Give the position of every malaria parasite.
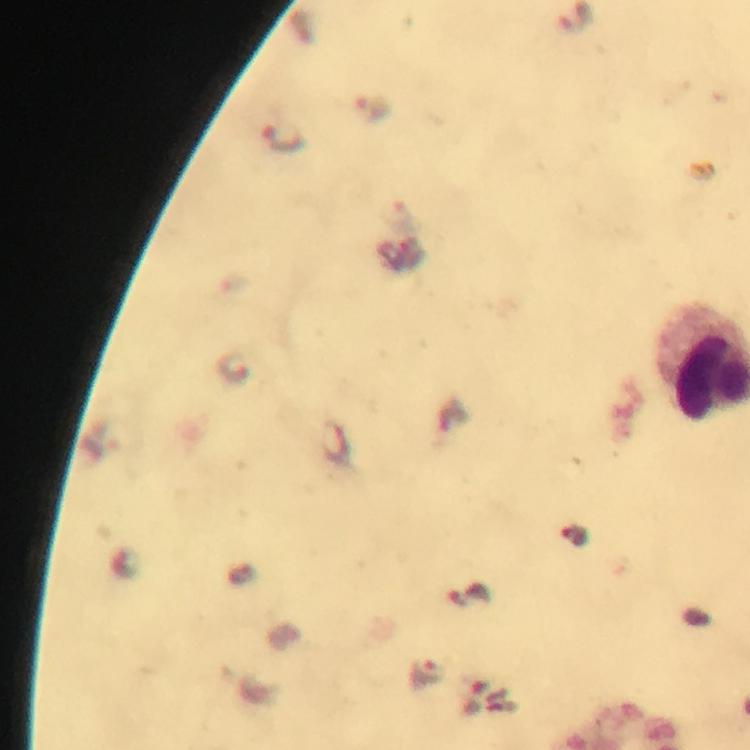

Approximate centers as (x, y) in pixels.
Malaria parasites: (373, 106), (282, 139), (573, 537), (426, 673).

At 100x magnification. Cropped region of a single field of view. From a malaria diagnostic workup. Thick smear. Smartphone photograph taken through a microscope. Immersion oil applied. Image is 750×750 pixels. Giemsa stain.